Describe the morphology of the red blood cells.
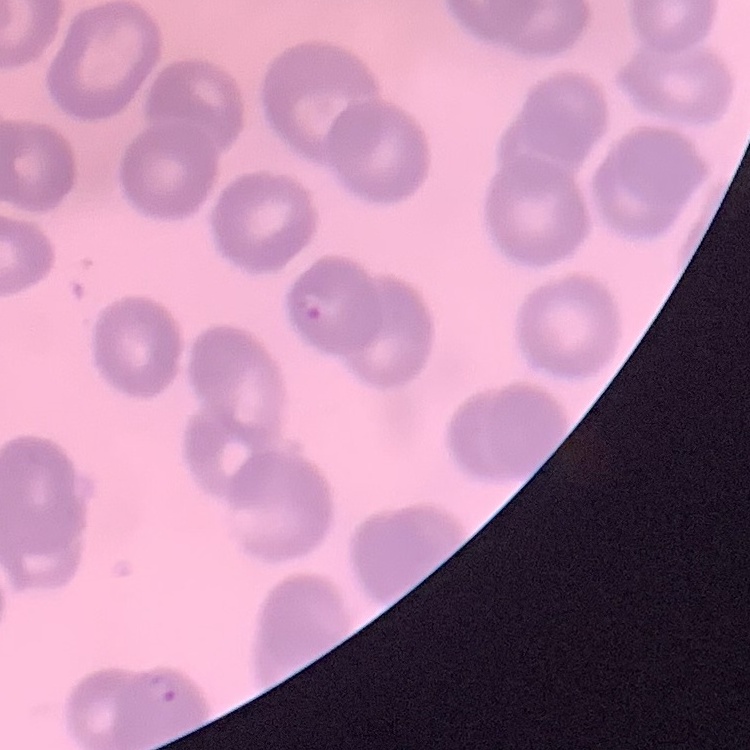
They show no rouleaux formation.

stain = Field's or Giemsa
preparation = thin peripheral smear
image type = one tile cut from a larger photomicrograph